Name the blood parasite species.
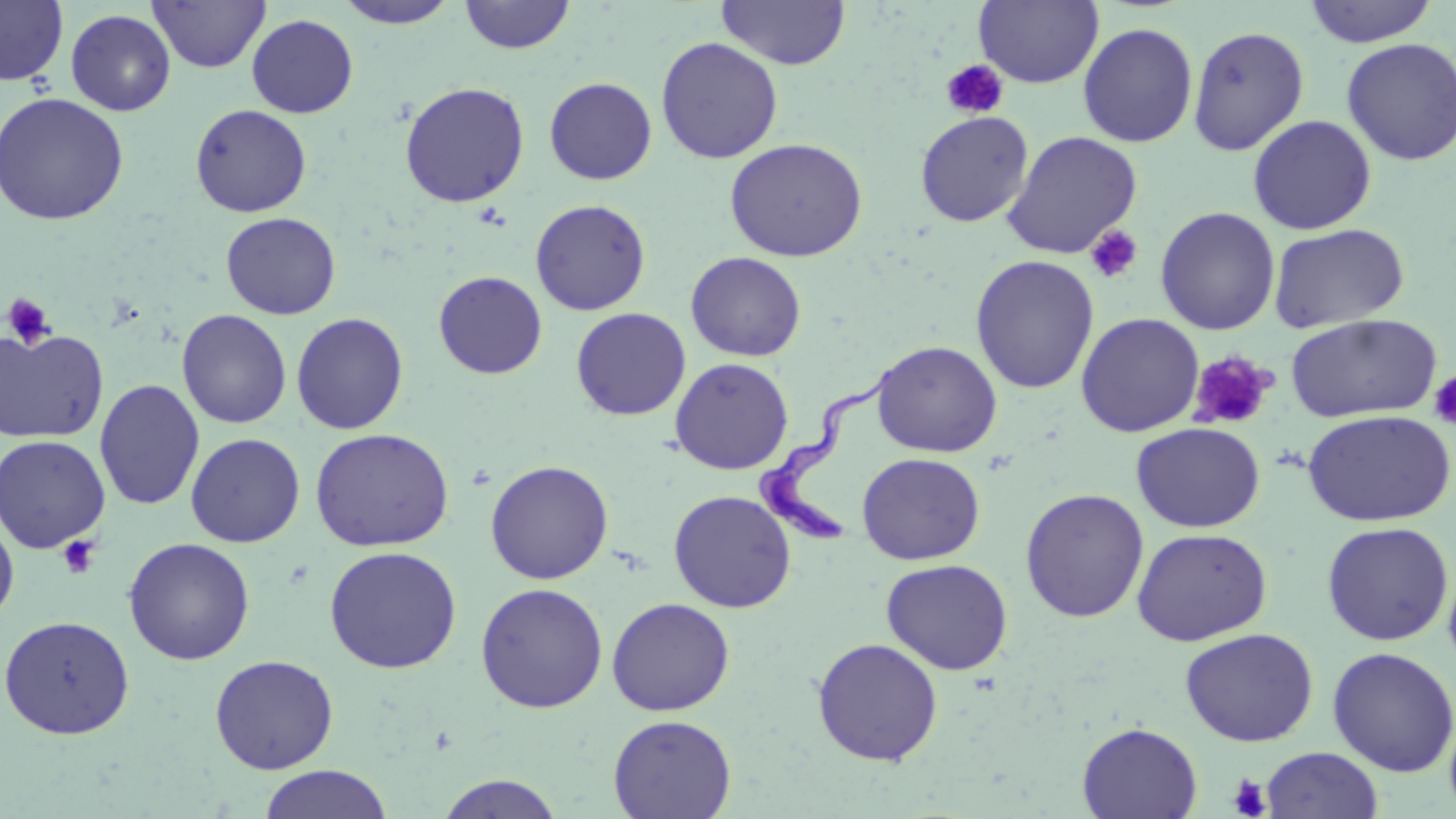

Trypanosoma brucei.

field_of_view: one of a larger specimen
magnification: 1000x
image_size: 1456×819 pixels
platelet_locations: 'approximate bounding boxes as (x1,y1)-(x2,y2) corner pairs in pixels: (940,59)-(1009,120), (1084,224)-(1143,284), (2,293)-(56,349), (1187,351)-(1275,432), (1428,371)-(1456,431), (57,536)-(100,580), (1227,774)-(1271,818)'
preparation: thin blood smear
uninfected_red_blood_cell_locations: 'approximate bounding boxes as (x1,y1)-(x2,y2) corner pairs in pixels: (0,0)-(68,87), (148,0)-(269,73), (716,0)-(850,70), (974,0)-(1104,88), (1302,0)-(1439,47), (333,1)-(463,29), (459,1)-(576,54), (65,9)-(176,116), (247,14)-(359,118), (1078,22)-(1198,147), (1187,24)-(1310,156), (656,36)-(783,164), (1341,38)-(1456,166), (544,77)-(657,185), (399,81)-(530,208), (0,92)-(129,225), (190,104)-(312,217), (915,110)-(1034,227), (1248,114)-(1377,235), (1001,129)-(1143,260), (725,137)-(868,262), (530,199)-(651,316), (1155,206)-(1280,335), (221,212)-(341,319), (1268,222)-(1410,333), (685,251)-(806,361), (970,255)-(1099,394), (433,270)-(547,379), (571,307)-(691,421), (176,308)-(292,429), (291,312)-(409,434), (1076,312)-(1205,437), (1285,313)-(1442,423), (0,327)-(109,443), (871,340)-(1002,457), (670,357)-(794,475), (94,378)-(205,510), (1302,409)-(1455,526), (1130,422)-(1266,533), (309,428)-(455,552), (185,432)-(305,547), (0,434)-(111,553), (857,452)-(986,565), (484,460)-(614,584), (1020,488)-(1149,623), (668,489)-(797,612), (0,511)-(19,627), (1321,521)-(1454,645), (1131,527)-(1272,646), (123,537)-(255,665), (324,545)-(462,674), (881,558)-(1013,675), (475,582)-(609,713), (606,597)-(735,716), (0,614)-(134,740), (1180,627)-(1319,746), (812,637)-(943,766), (1327,646)-(1456,776), (209,654)-(339,774), (608,714)-(736,819), (1077,721)-(1202,819), (1260,746)-(1384,819), (259,764)-(391,819), (434,773)-(566,818)'
modality: optical microscopy
stain: May-Grünwald-Giemsa
trypanosoma_brucei_locations: 'approximate bounding boxes as (x1,y1)-(x2,y2) corner pairs in pixels: (755,360)-(895,545)'